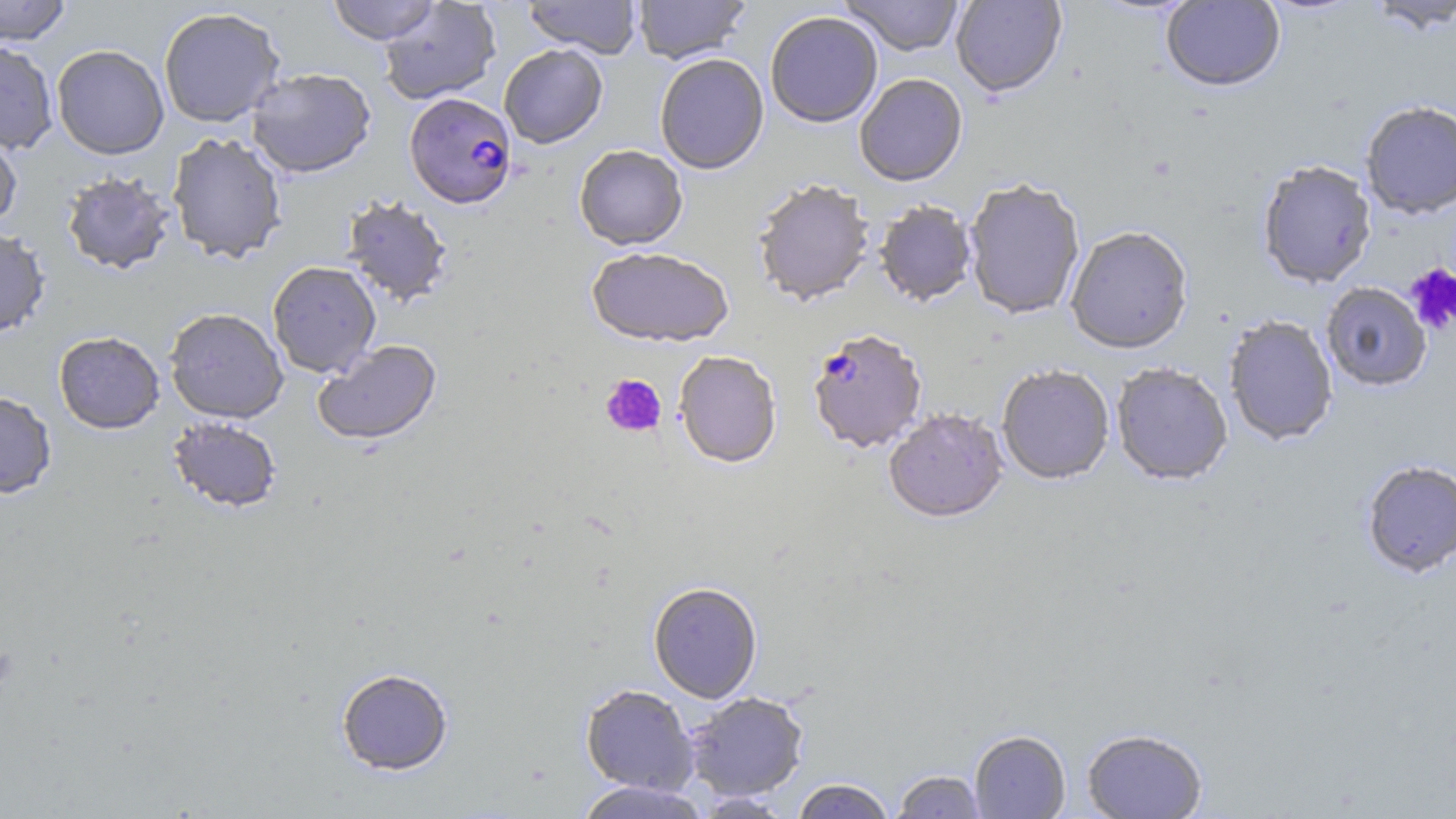
{
  "plasmodium_falciparum_infected_red_blood_cell_locations": "approximate bounding boxes as named x1/y1/x2/y2 corners in pixels: (x1=405, y1=94, x2=518, y2=210), (x1=807, y1=332, x2=927, y2=456)",
  "slide_level_diagnosis": "Plasmodium falciparum",
  "platelet_locations": "approximate bounding boxes as named x1/y1/x2/y2 corners in pixels: (x1=1405, y1=262, x2=1456, y2=335), (x1=600, y1=374, x2=666, y2=437)",
  "uninfected_red_blood_cell_locations": "approximate bounding boxes as named x1/y1/x2/y2 corners in pixels: (x1=0, y1=0, x2=71, y2=46), (x1=327, y1=0, x2=440, y2=45), (x1=524, y1=0, x2=641, y2=59), (x1=633, y1=0, x2=751, y2=65), (x1=838, y1=0, x2=965, y2=58), (x1=951, y1=0, x2=1067, y2=100), (x1=1161, y1=0, x2=1285, y2=93), (x1=1363, y1=0, x2=1456, y2=35), (x1=378, y1=1, x2=501, y2=105), (x1=158, y1=7, x2=285, y2=128), (x1=766, y1=14, x2=883, y2=129), (x1=0, y1=41, x2=59, y2=154), (x1=51, y1=44, x2=169, y2=160), (x1=499, y1=45, x2=608, y2=150), (x1=655, y1=55, x2=769, y2=176), (x1=246, y1=67, x2=376, y2=179), (x1=855, y1=75, x2=968, y2=189), (x1=1360, y1=102, x2=1456, y2=221), (x1=0, y1=125, x2=23, y2=233), (x1=167, y1=131, x2=288, y2=264), (x1=574, y1=147, x2=688, y2=252), (x1=1258, y1=163, x2=1376, y2=290), (x1=61, y1=171, x2=176, y2=276), (x1=753, y1=182, x2=875, y2=308), (x1=964, y1=182, x2=1085, y2=320), (x1=341, y1=196, x2=454, y2=308), (x1=874, y1=203, x2=977, y2=308), (x1=1066, y1=228, x2=1192, y2=357), (x1=0, y1=229, x2=51, y2=338), (x1=586, y1=250, x2=733, y2=349), (x1=267, y1=261, x2=381, y2=378), (x1=1320, y1=283, x2=1432, y2=393), (x1=164, y1=308, x2=288, y2=424), (x1=1224, y1=317, x2=1338, y2=447), (x1=54, y1=331, x2=165, y2=435), (x1=313, y1=340, x2=443, y2=448), (x1=674, y1=353, x2=782, y2=471), (x1=1111, y1=365, x2=1233, y2=488), (x1=997, y1=367, x2=1114, y2=487), (x1=0, y1=391, x2=57, y2=499), (x1=883, y1=411, x2=1008, y2=526), (x1=166, y1=417, x2=282, y2=513), (x1=1362, y1=462, x2=1456, y2=580), (x1=648, y1=584, x2=762, y2=704), (x1=336, y1=668, x2=453, y2=777), (x1=580, y1=685, x2=699, y2=796), (x1=685, y1=692, x2=809, y2=801), (x1=1082, y1=731, x2=1207, y2=819), (x1=969, y1=732, x2=1070, y2=818), (x1=891, y1=770, x2=987, y2=818), (x1=792, y1=779, x2=895, y2=819), (x1=573, y1=781, x2=711, y2=819)",
  "field_of_view": "single",
  "modality": "optical microscopy",
  "magnification": "1000x",
  "image_size": "1456×819 pixels",
  "stain": "May-Grünwald-Giemsa",
  "preparation": "thin blood smear"
}